Give the extent of all uninfected red blood cells.
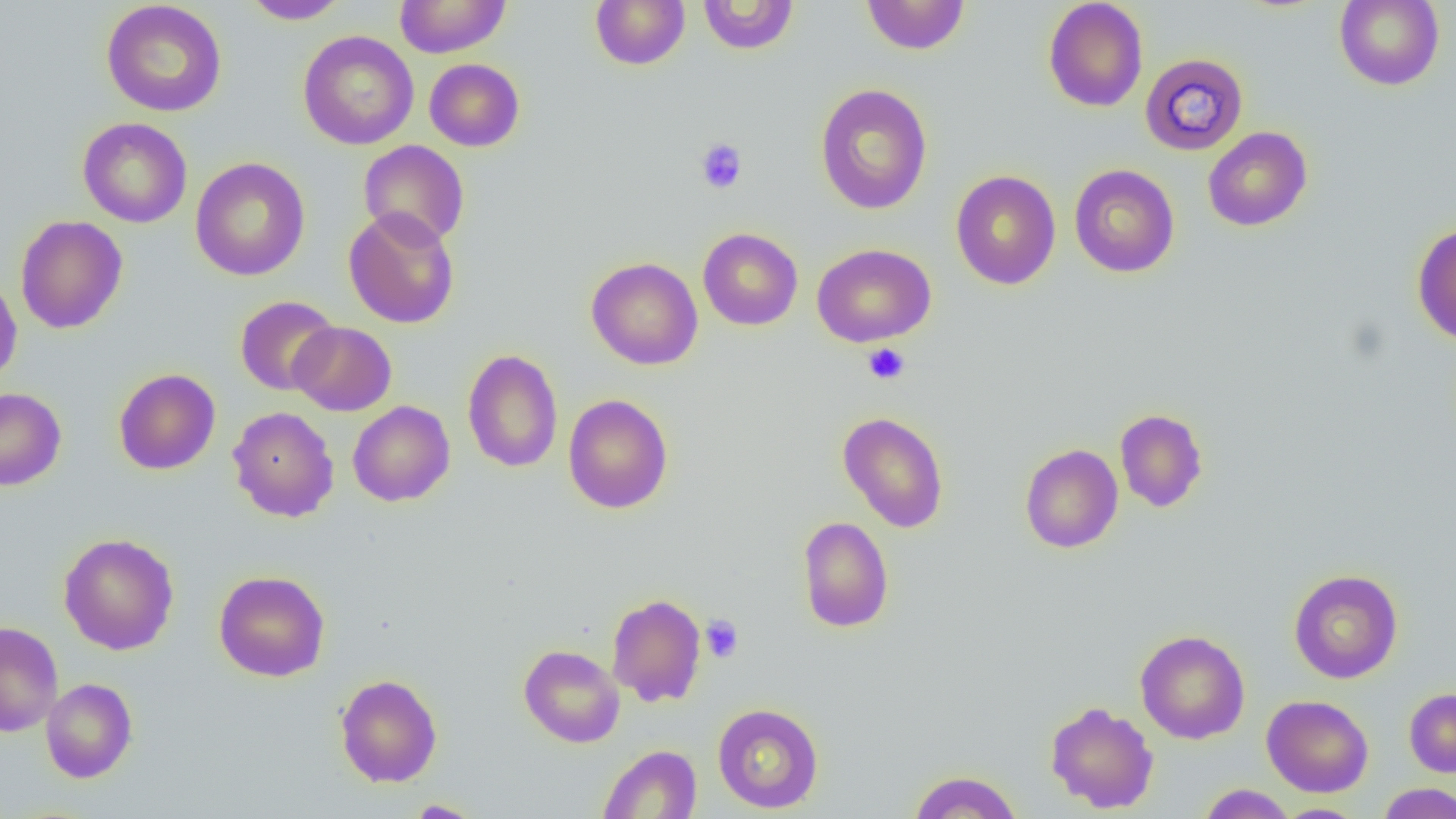

Approximate bounding boxes as named x1/y1/x2/y2 corners in pixels.
Uninfected red blood cells: (x1=240, y1=0, x2=351, y2=24), (x1=394, y1=0, x2=511, y2=58), (x1=590, y1=0, x2=690, y2=70), (x1=697, y1=0, x2=799, y2=55), (x1=861, y1=0, x2=970, y2=55), (x1=1043, y1=0, x2=1148, y2=112), (x1=1334, y1=0, x2=1445, y2=90), (x1=101, y1=1, x2=227, y2=117), (x1=298, y1=30, x2=419, y2=150), (x1=1139, y1=52, x2=1249, y2=156), (x1=424, y1=58, x2=525, y2=151), (x1=814, y1=84, x2=933, y2=214), (x1=78, y1=117, x2=192, y2=228), (x1=1203, y1=126, x2=1313, y2=231), (x1=358, y1=140, x2=470, y2=248), (x1=190, y1=157, x2=310, y2=281), (x1=1069, y1=163, x2=1180, y2=278), (x1=950, y1=170, x2=1061, y2=290), (x1=343, y1=208, x2=460, y2=329), (x1=15, y1=215, x2=128, y2=334), (x1=1411, y1=222, x2=1456, y2=345), (x1=698, y1=227, x2=803, y2=330), (x1=812, y1=243, x2=936, y2=347), (x1=586, y1=257, x2=703, y2=370), (x1=0, y1=273, x2=22, y2=387), (x1=235, y1=295, x2=340, y2=396), (x1=289, y1=322, x2=397, y2=416), (x1=462, y1=348, x2=563, y2=473), (x1=114, y1=368, x2=220, y2=475), (x1=0, y1=387, x2=66, y2=491), (x1=562, y1=394, x2=673, y2=514), (x1=348, y1=400, x2=455, y2=506), (x1=228, y1=407, x2=339, y2=522), (x1=1115, y1=408, x2=1209, y2=512), (x1=838, y1=411, x2=949, y2=533), (x1=1019, y1=444, x2=1123, y2=553), (x1=797, y1=516, x2=894, y2=633), (x1=58, y1=533, x2=179, y2=655), (x1=1288, y1=569, x2=1403, y2=683), (x1=214, y1=570, x2=330, y2=681), (x1=606, y1=593, x2=707, y2=707), (x1=0, y1=621, x2=63, y2=737), (x1=1135, y1=629, x2=1250, y2=744), (x1=518, y1=644, x2=625, y2=747), (x1=335, y1=674, x2=442, y2=787), (x1=41, y1=678, x2=137, y2=783), (x1=1404, y1=688, x2=1456, y2=777), (x1=1262, y1=694, x2=1374, y2=797), (x1=1045, y1=700, x2=1159, y2=814), (x1=712, y1=703, x2=824, y2=813), (x1=598, y1=744, x2=702, y2=818), (x1=908, y1=770, x2=1023, y2=818), (x1=1378, y1=783, x2=1456, y2=819), (x1=1197, y1=784, x2=1297, y2=819), (x1=404, y1=799, x2=484, y2=817), (x1=1273, y1=803, x2=1368, y2=818).

Summary:
  - Platelet locations: (x1=695, y1=138, x2=747, y2=194), (x1=863, y1=343, x2=910, y2=385), (x1=700, y1=615, x2=744, y2=662)
  - Slide-level diagnosis: no evidence of blood parasites
  - Preparation: thin blood film
  - Field of view: one of a larger specimen
  - Modality: optical microscopy
  - Image size: 1456×819 pixels
  - Magnification: 1000x